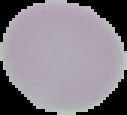
Summary:
  - Image size: 127×115 pixels
  - Result: no malaria parasites detected
  - Preparation: thin blood smear
  - Image type: segmented cell region on a black background